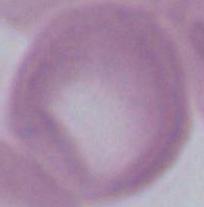 Photomicrograph. An erythrocyte is seen. Captured at 1000x magnification.